Assess for malaria.
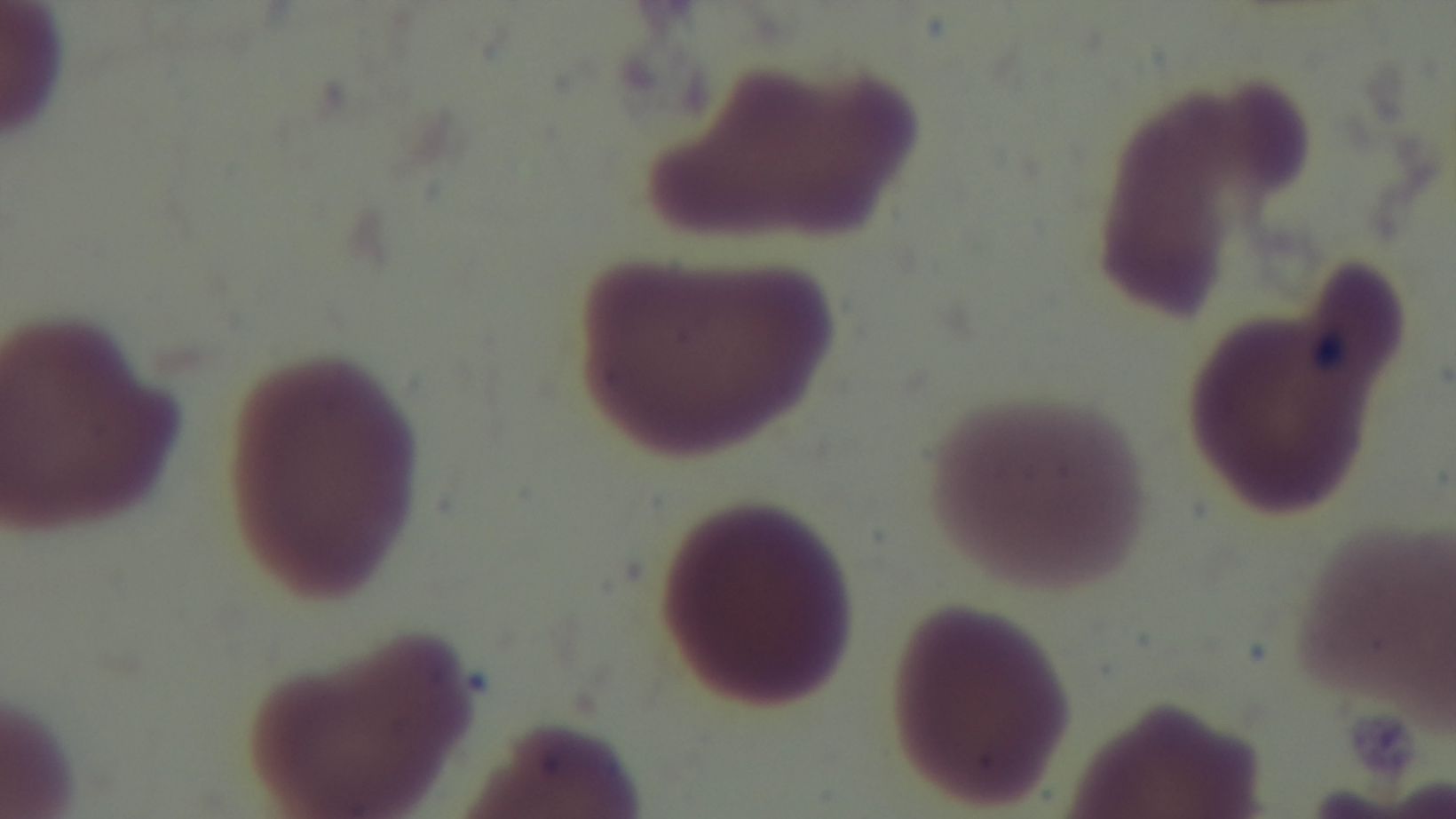
It is uninfected.

{
  "capture": "mounted 4K digital camera",
  "preparation": "thin blood film",
  "modality": "light microscopy",
  "field_of_view": "single",
  "objective": "100x oil immersion",
  "stain": "Giemsa"
}